Locate and identify every blood parasite.
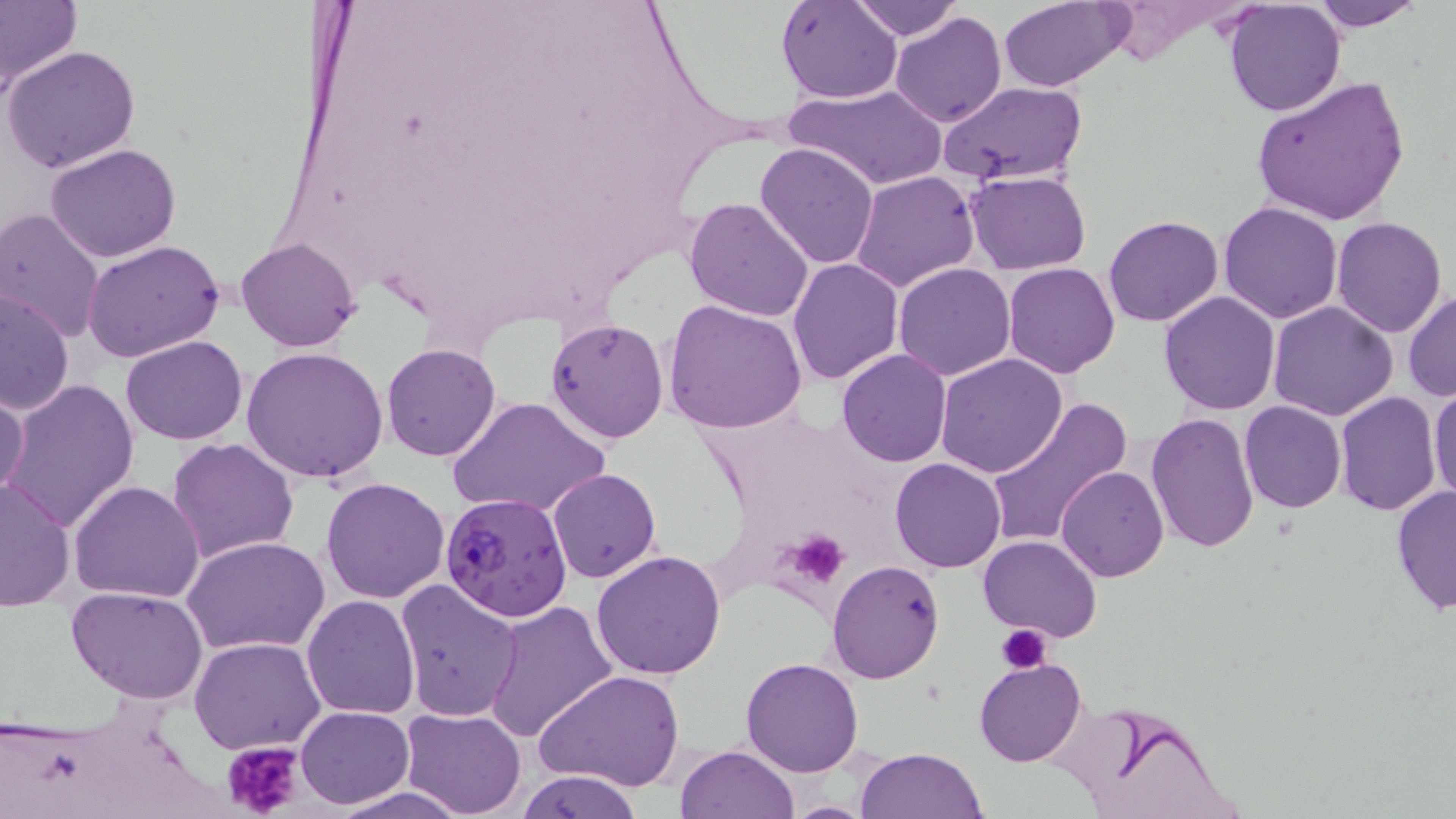

Approximate bounding boxes as [x1, y1, x2, y2] in pixels.
Plasmodium falciparum-infected red blood cells: [439, 493, 572, 622].
No Plasmodium ovale, Plasmodium malariae, Plasmodium vivax, Babesia divergens, or Trypanosoma brucei observed.

Uninfected red blood cell locations: [0, 0, 79, 97], [776, 0, 902, 104], [849, 0, 963, 42], [1223, 0, 1346, 116], [1307, 0, 1425, 31], [999, 1, 1131, 91], [890, 13, 1007, 127], [5, 46, 140, 173], [1250, 74, 1411, 227], [939, 80, 1087, 186], [785, 83, 949, 191], [754, 141, 880, 269], [45, 144, 183, 262], [852, 171, 981, 292], [966, 171, 1092, 273], [836, 175, 997, 384], [684, 195, 816, 321], [1218, 201, 1344, 322], [0, 207, 106, 345], [1102, 214, 1225, 327], [1330, 216, 1448, 338], [236, 237, 361, 352], [81, 240, 225, 363], [787, 259, 904, 386], [1003, 262, 1119, 378], [893, 263, 1016, 380], [1403, 289, 1456, 401], [0, 290, 74, 417], [1158, 291, 1281, 416], [662, 298, 808, 434], [1268, 300, 1398, 420], [546, 318, 670, 441], [121, 334, 248, 446], [381, 343, 502, 461], [243, 347, 388, 484], [836, 349, 953, 467], [935, 353, 1068, 478], [3, 378, 141, 534], [1430, 381, 1456, 504], [0, 385, 29, 508], [1335, 390, 1441, 514], [446, 396, 610, 521], [984, 396, 1131, 549], [1239, 401, 1347, 513], [1146, 412, 1257, 554], [167, 437, 298, 565], [890, 458, 1007, 573], [1057, 465, 1170, 581], [547, 467, 662, 582], [0, 475, 74, 610], [319, 477, 450, 603], [67, 480, 205, 603], [1391, 486, 1455, 616], [979, 533, 1102, 642], [182, 534, 331, 658], [592, 549, 727, 681], [827, 559, 945, 683], [395, 580, 524, 722], [66, 585, 208, 703], [301, 594, 419, 719], [484, 600, 618, 744], [190, 638, 327, 755], [740, 657, 864, 776], [974, 658, 1086, 767], [535, 670, 684, 792], [1056, 700, 1243, 819], [297, 706, 414, 807], [400, 707, 527, 818], [674, 745, 800, 819], [855, 747, 987, 819], [515, 770, 644, 818], [326, 786, 468, 819], [778, 801, 884, 818]. Platelet locations: [785, 530, 850, 588], [996, 625, 1051, 672], [222, 740, 306, 819]. Slide-level diagnosis: Plasmodium falciparum. Thin blood smear. Optical microscopy. One field of a larger specimen. May-Grünwald-Giemsa stain. Image is 1456×819 pixels. 1000x magnification.